Locate and identify every blood parasite.
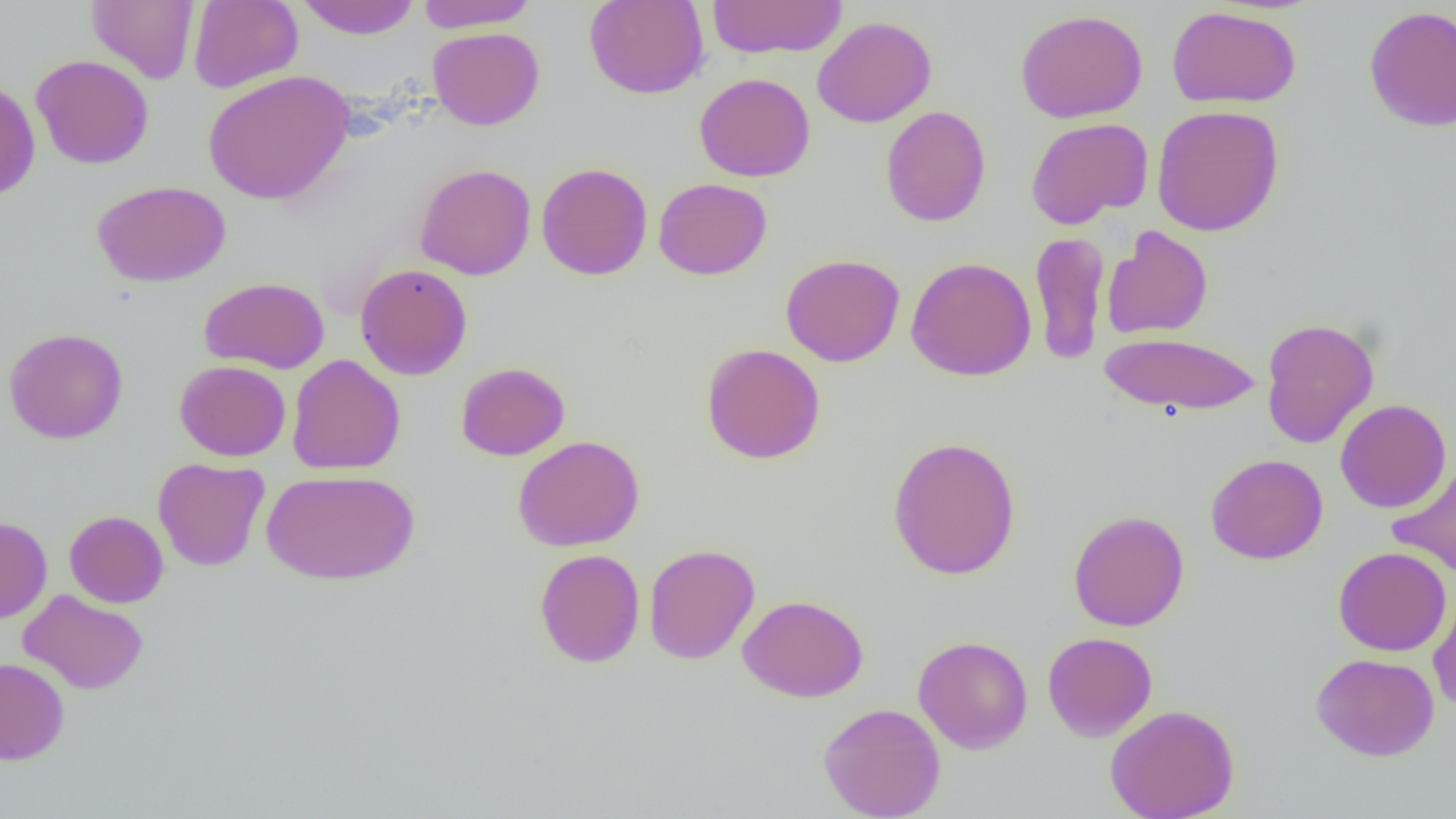
No blood parasites observed.

Summary:
  - Coordinate format: approximate bounding boxes as [x1, y1, x2, y2] in pixels
  - Uninfected red blood cell locations: [87, 0, 199, 84], [188, 0, 303, 93], [296, 0, 421, 39], [416, 0, 537, 32], [584, 0, 709, 99], [706, 0, 847, 59], [1363, 4, 1456, 132], [1167, 5, 1302, 109], [1015, 8, 1148, 123], [812, 15, 937, 127], [428, 27, 545, 130], [31, 54, 154, 170], [202, 70, 354, 205], [694, 73, 815, 181], [0, 79, 41, 201], [880, 105, 991, 226], [1151, 105, 1285, 237], [1026, 117, 1153, 229], [537, 162, 653, 280], [414, 163, 536, 280], [653, 177, 772, 280], [92, 180, 231, 287], [1101, 225, 1213, 339], [1029, 231, 1109, 366], [780, 253, 906, 367], [906, 256, 1036, 381], [355, 263, 472, 380], [199, 276, 330, 374], [1260, 317, 1379, 448], [3, 327, 128, 444], [1100, 331, 1261, 415], [701, 343, 826, 464], [286, 354, 405, 474], [174, 360, 291, 461], [455, 362, 570, 461], [1335, 398, 1452, 513], [512, 435, 645, 551], [886, 436, 1022, 580], [1206, 453, 1328, 564], [153, 457, 270, 571], [1388, 461, 1456, 579], [261, 468, 419, 585], [65, 510, 168, 608], [1068, 510, 1189, 632], [0, 516, 52, 624], [644, 543, 760, 664], [1333, 546, 1451, 656], [534, 548, 645, 668], [1428, 588, 1456, 711], [18, 589, 149, 695], [737, 594, 869, 702], [1042, 632, 1157, 742], [913, 635, 1033, 754], [1310, 652, 1440, 761], [0, 657, 70, 765], [818, 702, 946, 818], [1105, 703, 1240, 819]
  - Slide-level diagnosis: no evidence of blood parasites
  - Preparation: thin blood film
  - Field of view: one of a larger specimen
  - Image size: 1456×819 pixels
  - Modality: optical microscopy
  - Magnification: 1000x